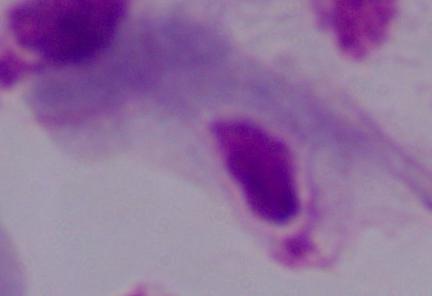

A trichomonad is seen. Captured at 1000x magnification. Micrograph.